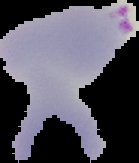 Image is 139×163 pixels. The area outside the segmented cell region is set to black. From a thin blood smear. Result: malaria parasites identified.